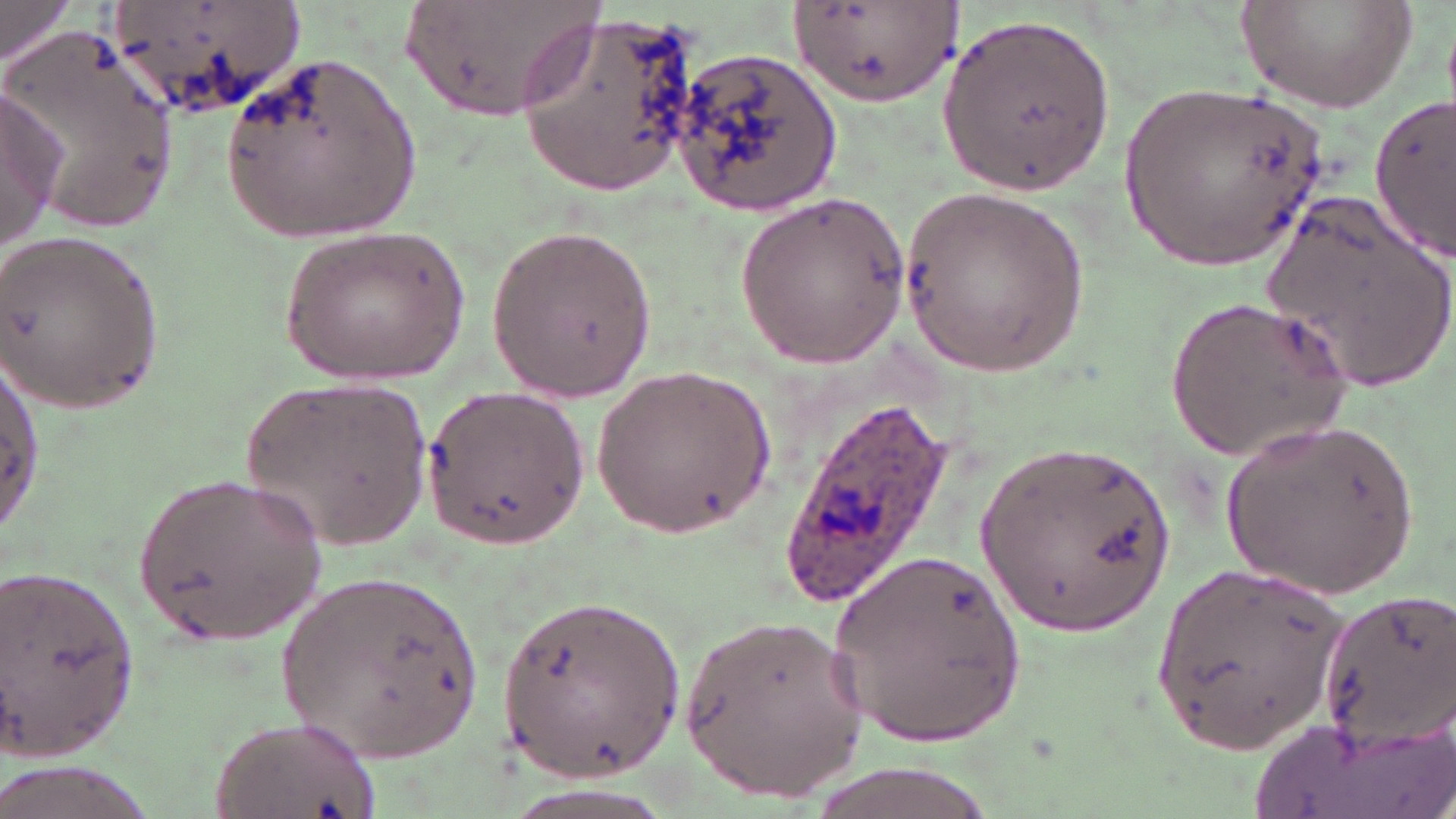

Approximate bounding boxes as [x1, y1, x2, y2] in pixels. Uninfected red blood cell locations: [0, 0, 73, 66], [109, 0, 306, 118], [404, 0, 604, 122], [1236, 0, 1422, 114], [791, 2, 956, 108], [516, 10, 706, 197], [942, 14, 1119, 197], [8, 27, 183, 236], [675, 47, 844, 214], [219, 51, 420, 251], [1118, 81, 1335, 277], [0, 85, 64, 258], [1371, 102, 1455, 257], [900, 183, 1090, 380], [735, 193, 911, 367], [1262, 194, 1456, 392], [280, 223, 468, 385], [485, 223, 659, 404], [1, 229, 164, 411], [1164, 294, 1351, 465], [1, 361, 43, 530], [595, 365, 778, 537], [244, 372, 435, 556], [425, 385, 590, 552], [1220, 419, 1415, 600], [976, 437, 1181, 639], [134, 469, 327, 642], [830, 545, 1028, 751], [4, 565, 147, 758], [1154, 565, 1348, 752], [277, 569, 484, 764], [1316, 584, 1456, 752], [496, 595, 689, 777], [676, 614, 876, 794], [211, 717, 384, 819], [795, 762, 1008, 819]. Plasmodium ovale-infected red blood cell locations: [774, 393, 960, 609]. Slide-level diagnosis: Plasmodium ovale. Single field of view. Image is 1456×819 pixels. Thin blood film. May-Grünwald-Giemsa-stained preparation. Captured at 1000x magnification. Light microscopy.